State which parasite is depicted.
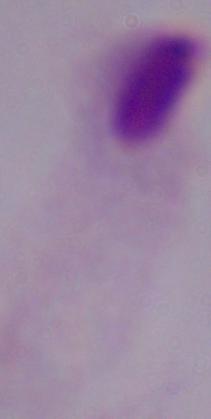
A trichomonad.

Summary:
  - Magnification: 1000x
  - Modality: photomicrograph